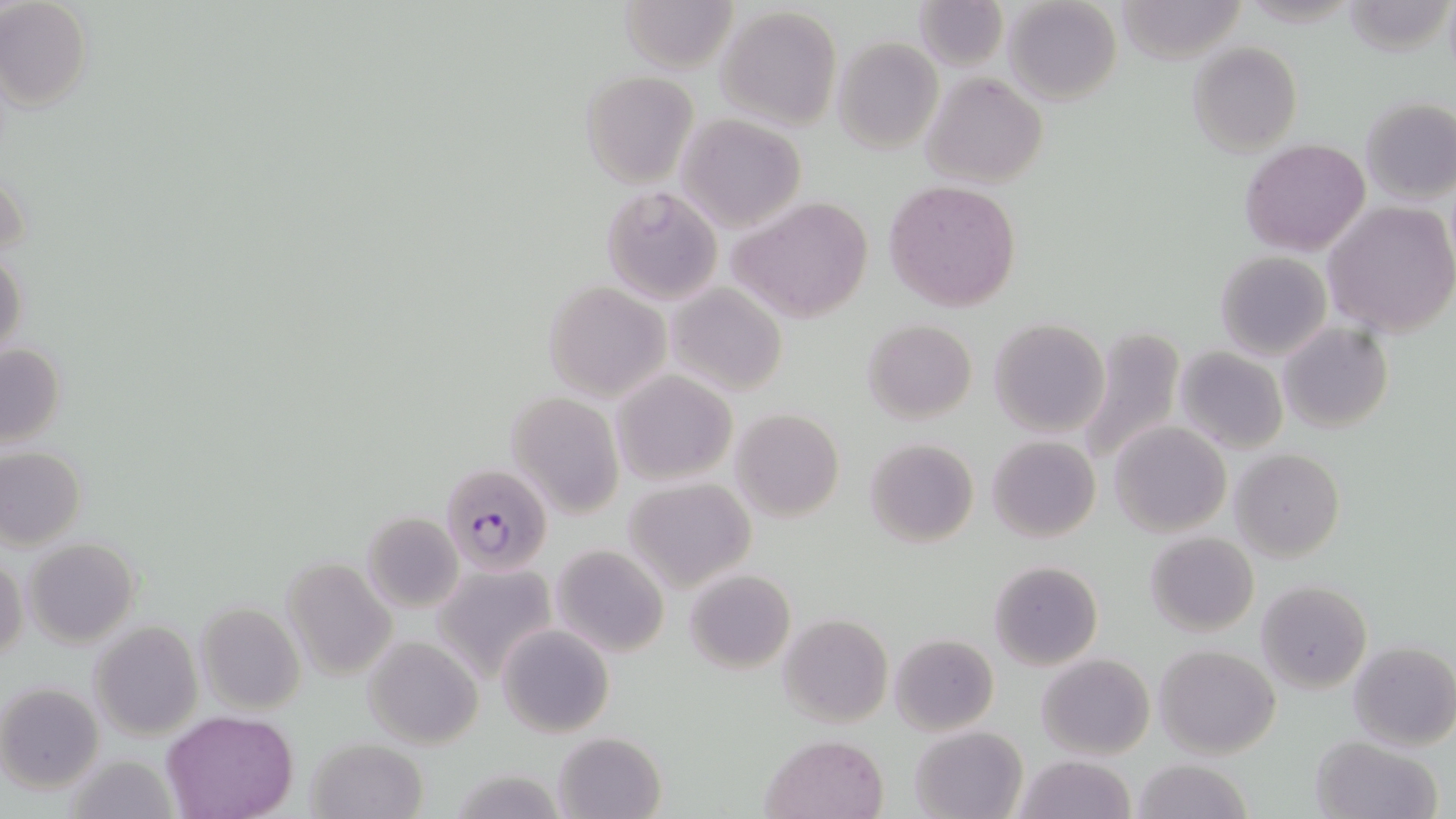

slide_level_diagnosis: Plasmodium falciparum
image_size: 1456×819 pixels
uninfected_red_blood_cell_locations: 'approximate bounding boxes as (x1,y1)-(x2,y2) corner pairs in pixels: (0,0)-(91,111), (913,0)-(1009,72), (1003,0)-(1123,105), (1117,0)-(1247,65), (1345,0)-(1453,57), (618,1)-(737,72), (716,5)-(842,130), (831,36)-(942,155), (1187,41)-(1303,156), (581,70)-(700,189), (921,73)-(1048,189), (1360,98)-(1456,205), (675,113)-(806,232), (1241,138)-(1370,256), (1,167)-(28,262), (883,180)-(1023,314), (600,183)-(725,304), (728,195)-(874,324), (1324,202)-(1456,337), (0,250)-(27,360), (1216,250)-(1333,360), (544,282)-(670,401), (667,285)-(787,396), (863,318)-(978,423), (988,318)-(1110,437), (1278,321)-(1393,434), (1073,327)-(1185,471), (0,342)-(67,449), (1175,347)-(1288,454), (611,370)-(737,487), (507,391)-(625,519), (731,408)-(844,523), (1110,420)-(1231,537), (987,435)-(1101,543), (864,437)-(979,548), (0,446)-(86,549), (1230,448)-(1344,563), (624,478)-(756,591), (363,511)-(463,612), (1145,531)-(1259,638), (23,537)-(140,647), (551,545)-(669,658), (1,553)-(26,665), (281,556)-(397,677), (988,560)-(1103,670), (432,561)-(560,681), (685,568)-(795,673), (1256,579)-(1373,697), (196,603)-(305,713), (778,613)-(892,728), (89,621)-(202,741), (497,623)-(615,737), (889,634)-(998,735), (364,635)-(483,749), (1348,641)-(1456,751), (1154,644)-(1280,758), (1036,653)-(1155,760), (1,683)-(104,791), (163,711)-(298,819), (910,727)-(1027,819), (553,732)-(669,819), (762,734)-(889,818), (1308,736)-(1443,819), (306,737)-(428,819), (65,753)-(178,819), (1015,753)-(1136,819), (1131,758)-(1255,818)'
modality: light microscopy
stain: May-Grünwald-Giemsa
preparation: thin blood smear
field_of_view: single
plasmodium_falciparum_infected_red_blood_cell_locations: 'approximate bounding boxes as (x1,y1)-(x2,y2) corner pairs in pixels: (440,463)-(555,576)'
magnification: 1000x